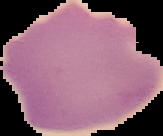

malaria_status: uninfected
image_size: 163×136 pixels
preparation: thin blood film
image_type: segmented cell region with the area outside set to black